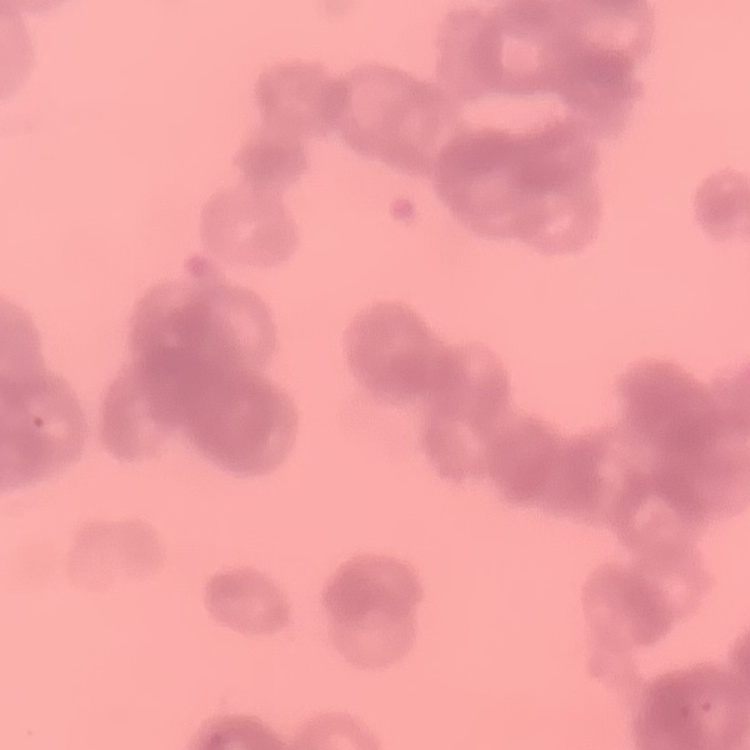

{
  "red_blood_cell_morphology": "rouleaux formation",
  "preparation": "thin peripheral smear",
  "image_type": "square crop of a larger photomicrograph",
  "stain": "Field's or Giemsa"
}